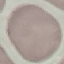

Summary:
  - Result: negative for malaria parasites
  - Preparation: thin smear
  - Image type: cell patch, automatically extracted from a larger field of view and resized to 64 × 64 pixels
  - Stain: Giemsa
  - Capture: smartphone through the microscope eyepiece